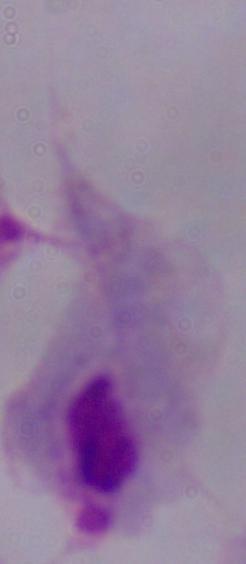

{
  "modality": "micrograph",
  "magnification": "1000x",
  "identification": "trichomonad"
}